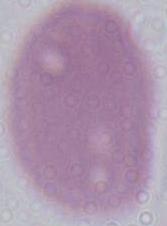
magnification = 1000x
identification = red blood cell
modality = micrograph